Locate every Plasmodium parasite and every leukocyte.
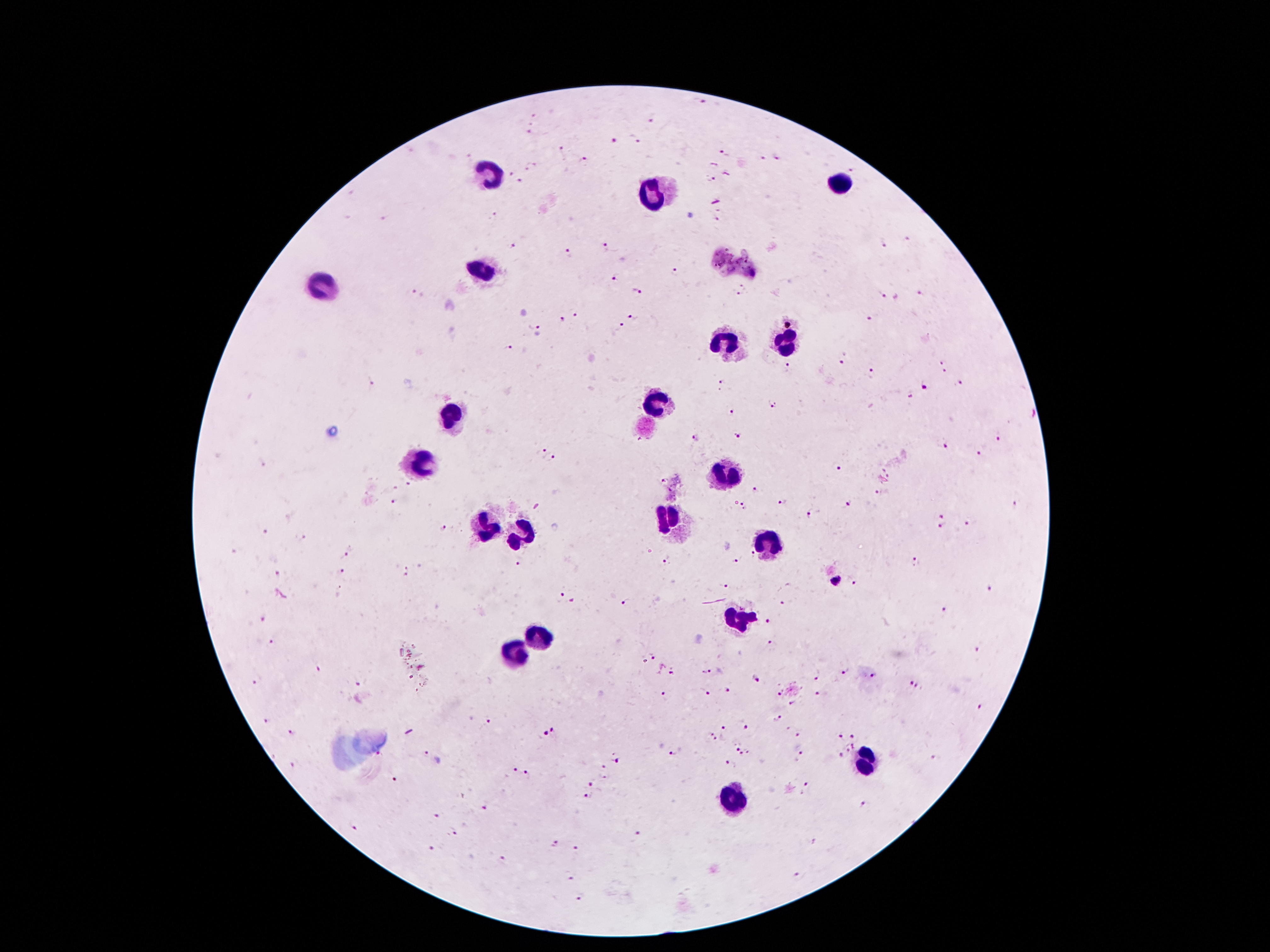
Approximate centers as (x, y) in pixels.
Plasmodium parasites: (703, 101), (650, 119), (529, 133), (635, 139), (614, 140), (563, 150), (723, 153), (761, 158), (777, 159), (585, 161), (855, 171), (710, 178), (520, 181), (495, 216), (719, 217), (385, 218), (907, 239), (883, 242), (604, 245), (513, 246), (569, 254), (675, 272), (618, 277), (743, 290), (636, 291), (412, 293), (882, 294), (921, 295), (574, 313), (633, 317), (562, 320), (792, 320), (868, 320), (534, 324), (619, 325), (508, 347), (842, 361), (941, 362), (789, 368), (945, 371), (871, 373), (372, 383), (721, 383), (960, 383), (926, 388), (911, 397), (772, 405), (731, 411), (739, 436), (697, 437), (999, 438), (945, 445), (538, 450), (980, 451), (552, 459), (260, 464), (837, 468), (408, 485), (755, 487), (878, 495), (392, 501), (783, 502), (849, 503), (1016, 504), (745, 506), (810, 512), (943, 515), (967, 523), (442, 527), (943, 527), (266, 533), (301, 537), (346, 554), (753, 556), (734, 561), (916, 562), (667, 563), (519, 566), (339, 570), (406, 574), (278, 575), (837, 581), (856, 581), (723, 586), (990, 588), (560, 595), (625, 601), (782, 602), (946, 609), (262, 620), (767, 621), (271, 641), (769, 644), (978, 650), (653, 657), (846, 670), (671, 673), (706, 673), (872, 675), (817, 676), (756, 680), (910, 682), (256, 683), (358, 685), (918, 687), (726, 691), (703, 692), (778, 694), (820, 694), (661, 695), (793, 704), (982, 708), (778, 716), (267, 720), (487, 723), (723, 726), (747, 727), (555, 731), (293, 734), (799, 734), (853, 734), (543, 735), (838, 735), (710, 737), (734, 744), (855, 744), (848, 749), (426, 753), (744, 754), (839, 754), (670, 755), (800, 755), (935, 758), (619, 759), (731, 764), (293, 765), (603, 768), (513, 770), (529, 775), (394, 779), (590, 782), (809, 786), (588, 797), (865, 807), (485, 808), (436, 814), (353, 828), (452, 831), (638, 835), (554, 844), (812, 844), (431, 849), (575, 850), (498, 860), (570, 877), (799, 879), (579, 899).
Leukocytes: (491, 173), (838, 185), (655, 192), (484, 274), (324, 284), (725, 340), (786, 343), (655, 404), (450, 415), (423, 461), (733, 471), (672, 520), (486, 525), (520, 532), (767, 545), (739, 617), (539, 638), (512, 656), (865, 760), (733, 800).

{
  "preparation": "thick blood film",
  "magnification": "100x",
  "capture": "smartphone camera through the microscope eyepiece",
  "patient_malaria_status": "infected with Plasmodium falciparum",
  "field_of_view": "one from this slide",
  "stain": "Giemsa",
  "image_size": "1270×952 pixels"
}